Outline each Plasmodium falciparum-infected red blood cell.
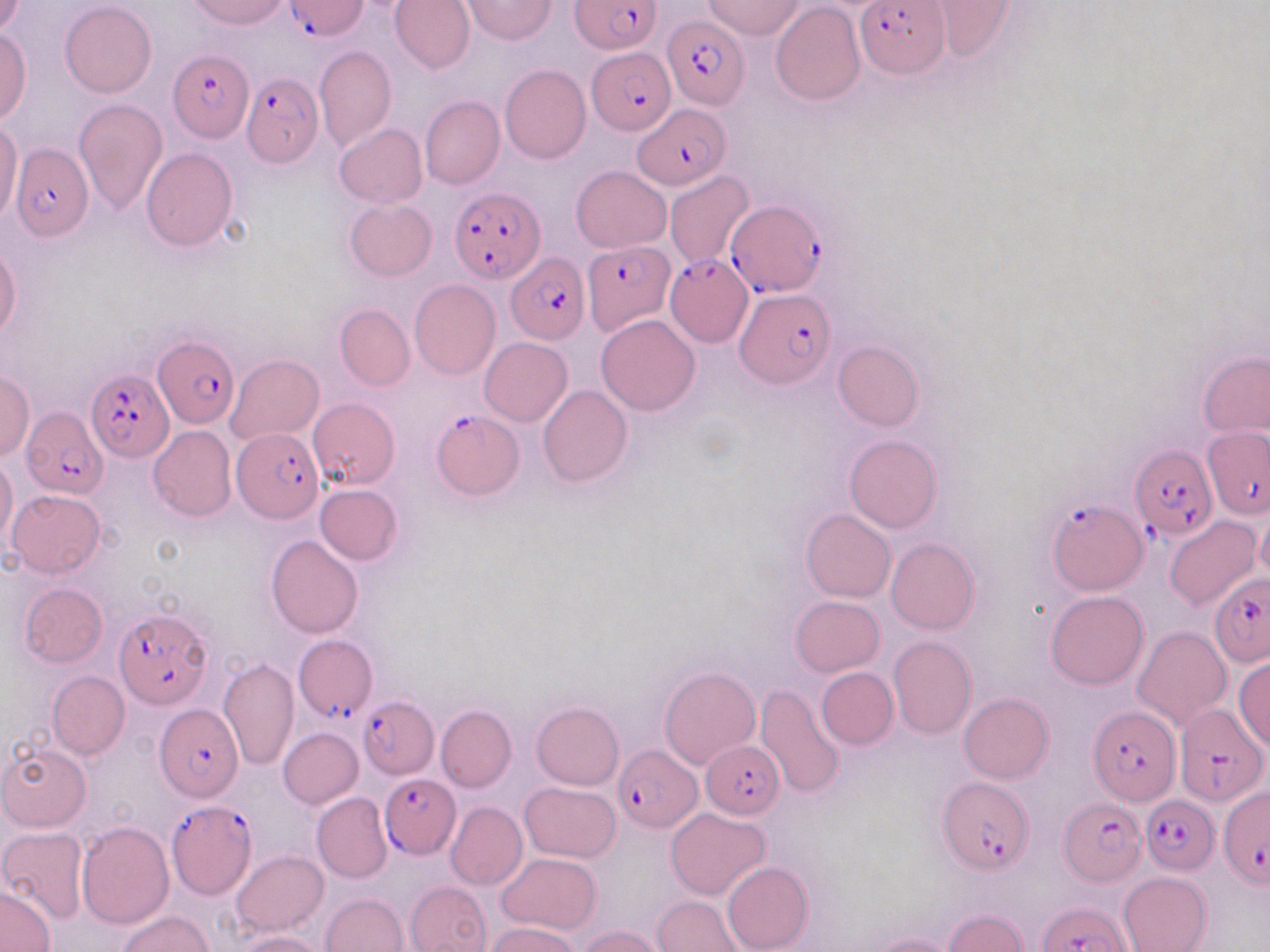
Approximate bounding boxes as (x1, y1, x2, y2) in pixels.
Plasmodium falciparum-infected red blood cells: (284, 0, 370, 40), (570, 0, 660, 53), (856, 0, 948, 77), (661, 12, 748, 110), (584, 47, 672, 131), (168, 49, 253, 142), (241, 73, 323, 167), (633, 104, 729, 188), (10, 142, 93, 242), (448, 186, 543, 284), (728, 198, 827, 296), (581, 241, 674, 335), (506, 253, 587, 342), (668, 255, 753, 347), (735, 289, 834, 389), (154, 335, 237, 432), (85, 368, 174, 463), (22, 407, 110, 499), (431, 409, 524, 499), (232, 427, 322, 523), (1204, 427, 1269, 519), (1127, 442, 1216, 542), (1047, 499, 1146, 594), (1209, 571, 1270, 666), (115, 607, 212, 708), (294, 637, 377, 724), (357, 694, 438, 777), (155, 704, 243, 801), (1175, 704, 1267, 805), (1087, 705, 1180, 804), (700, 739, 784, 818), (615, 744, 701, 831), (378, 772, 461, 858), (937, 777, 1034, 875), (1220, 787, 1270, 885), (1141, 794, 1219, 874), (1059, 797, 1146, 885), (166, 800, 257, 897), (1037, 899, 1134, 952).

slide-level diagnosis = Plasmodium falciparum
image size = 1270×952 pixels
preparation = thin blood film
modality = light microscopy
uninfected red blood cell locations = approximate bounding boxes as (x1, y1, x2, y2) in pixels: (0, 0, 28, 39), (186, 0, 290, 29), (392, 0, 475, 73), (464, 0, 557, 43), (704, 0, 806, 40), (59, 1, 157, 98), (770, 2, 866, 105), (923, 2, 1017, 60), (0, 28, 31, 122), (314, 46, 396, 152), (500, 65, 590, 164), (420, 96, 505, 189), (73, 98, 168, 218), (0, 117, 21, 223), (334, 123, 427, 207), (141, 147, 237, 251), (572, 165, 670, 251), (664, 171, 753, 268), (345, 197, 436, 280), (0, 244, 21, 340), (410, 279, 500, 379), (335, 304, 414, 391), (596, 314, 700, 416), (478, 337, 572, 425), (833, 341, 924, 431), (1198, 351, 1270, 439), (225, 354, 323, 444), (0, 371, 34, 459), (538, 385, 632, 486), (309, 397, 399, 488), (149, 426, 237, 522), (844, 435, 942, 533), (0, 453, 18, 553), (314, 483, 402, 565), (6, 490, 106, 578), (1255, 508, 1270, 583), (801, 509, 896, 603), (1165, 517, 1258, 610), (266, 535, 363, 638), (886, 537, 980, 635), (19, 582, 108, 667), (1046, 591, 1150, 690), (791, 595, 884, 676), (1132, 626, 1232, 731), (888, 636, 976, 739), (1234, 655, 1270, 752), (218, 657, 299, 771), (659, 666, 759, 769), (816, 667, 898, 750), (47, 671, 130, 759), (754, 685, 845, 800), (959, 693, 1053, 782), (531, 702, 623, 789), (436, 705, 516, 791), (278, 727, 363, 808), (0, 743, 90, 832), (519, 781, 621, 863), (310, 793, 393, 883), (446, 801, 527, 889), (666, 807, 770, 899), (77, 821, 173, 929), (1, 826, 89, 922), (233, 851, 328, 936), (496, 853, 603, 934), (722, 861, 811, 952), (1119, 871, 1212, 952), (406, 881, 491, 952), (0, 887, 56, 952), (321, 894, 407, 952), (653, 896, 742, 951), (943, 909, 1029, 951), (118, 911, 216, 952), (487, 922, 581, 952), (577, 925, 667, 952), (236, 930, 328, 952), (867, 933, 960, 952)
magnification = 1000x
stain = May-Grünwald-Giemsa
field of view = single